State which parasite is depicted.
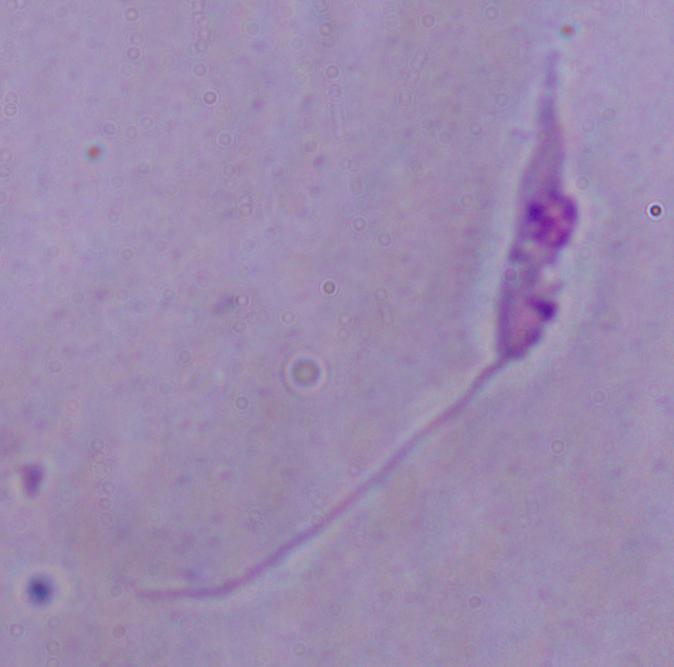
Leishmania.

Photomicrograph. Captured at 1000x magnification.